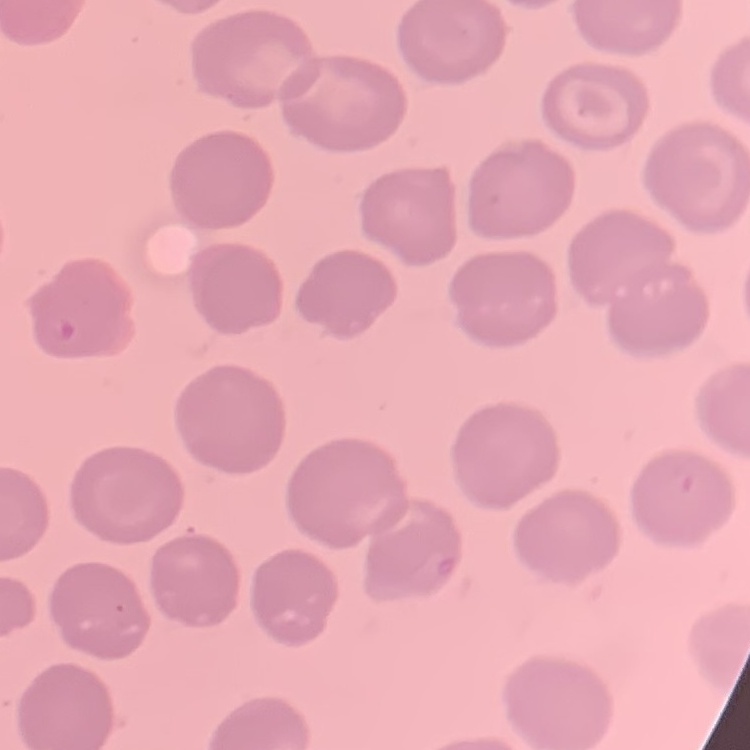
Summary:
  - Erythrocyte morphology: no rouleaux formation
  - Preparation: thin blood smear
  - Image type: square crop of a larger photomicrograph
  - Stain: Field's or Giemsa